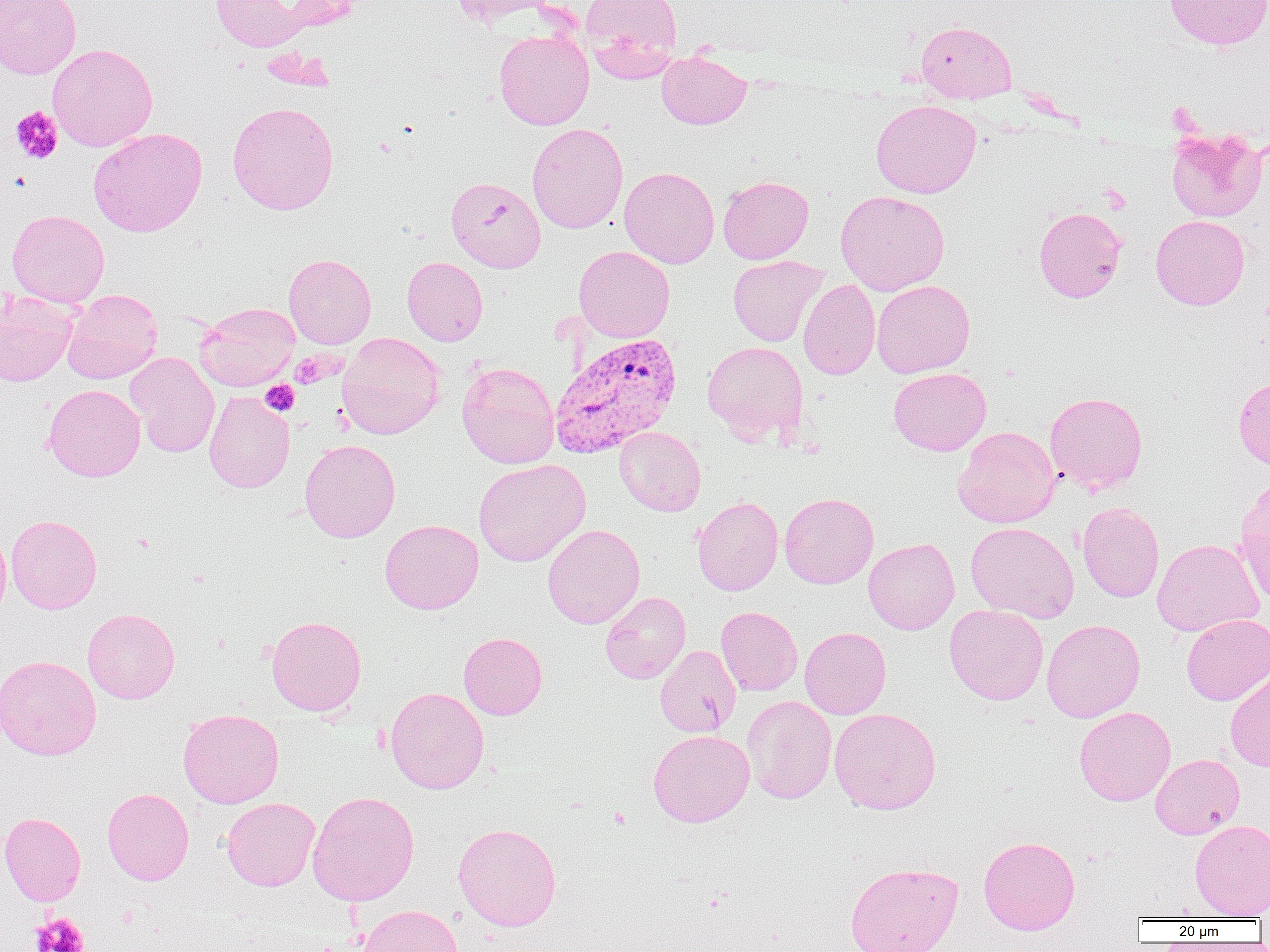

Plasmodium vivax-infected red blood cell locations = approximate bounding boxes as (x1, y1, x2, y2) in pixels: (549, 333, 682, 458)
slide-level diagnosis = Plasmodium vivax
image size = 1270×952 pixels
field of view = one of a larger specimen
magnification = 1000x
uninfected red blood cell locations = approximate bounding boxes as (x1, y1, x2, y2) in pixels: (0, 0, 81, 80), (209, 0, 322, 52), (450, 0, 557, 25), (579, 0, 683, 80), (1165, 0, 1270, 50), (915, 21, 1017, 103), (494, 29, 594, 130), (47, 43, 158, 151), (656, 50, 752, 129), (870, 99, 981, 198), (227, 101, 339, 215), (527, 123, 628, 234), (1165, 127, 1267, 222), (88, 128, 208, 237), (619, 166, 719, 268), (718, 175, 814, 264), (446, 176, 545, 272), (835, 190, 950, 295), (1033, 207, 1127, 303), (7, 209, 109, 307), (1151, 215, 1250, 310), (574, 246, 675, 342), (284, 253, 376, 349), (728, 255, 827, 347), (402, 256, 488, 345), (798, 279, 881, 380), (871, 279, 975, 378), (62, 288, 163, 383), (0, 291, 78, 386), (195, 302, 299, 391), (337, 332, 444, 440), (702, 341, 809, 445), (126, 352, 219, 458), (457, 361, 560, 468), (889, 368, 991, 455), (1233, 377, 1270, 470), (43, 384, 145, 481), (204, 390, 295, 493), (1045, 391, 1148, 494), (614, 426, 706, 516), (953, 426, 1059, 528), (300, 439, 401, 543), (473, 459, 591, 567), (1235, 482, 1270, 603), (779, 492, 879, 588), (692, 496, 783, 596), (1077, 501, 1165, 603), (6, 514, 102, 614), (380, 519, 483, 614), (965, 522, 1078, 623), (543, 524, 645, 629), (0, 525, 11, 624), (863, 538, 959, 634), (1152, 539, 1264, 636), (600, 591, 691, 684), (944, 604, 1048, 705), (716, 606, 803, 695), (82, 608, 180, 704), (1181, 614, 1270, 705), (266, 615, 366, 716), (1041, 619, 1145, 722), (800, 627, 891, 719), (458, 632, 547, 720), (655, 644, 741, 738), (0, 655, 101, 760), (1225, 672, 1270, 771), (385, 686, 489, 794), (741, 695, 837, 804), (1074, 706, 1176, 806), (829, 708, 941, 815), (178, 709, 284, 808), (648, 729, 754, 826), (1150, 753, 1244, 839), (102, 788, 194, 885), (308, 790, 419, 906), (221, 797, 320, 891), (0, 812, 86, 906), (1190, 819, 1270, 919), (453, 822, 561, 931), (978, 835, 1080, 934), (844, 861, 963, 952), (358, 904, 463, 952)
modality = light microscopy
preparation = thin blood film
platelet locations = approximate bounding boxes as (x1, y1, x2, y2) in pixels: (11, 106, 63, 164), (291, 352, 333, 388), (260, 380, 300, 416), (31, 913, 89, 952)